Report the malaria status of this cell.
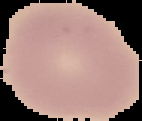

It is uninfected.

Cell region segmented out of the field of view; the surrounding area is masked to black. From a thin blood smear. Image is 142×121 pixels.